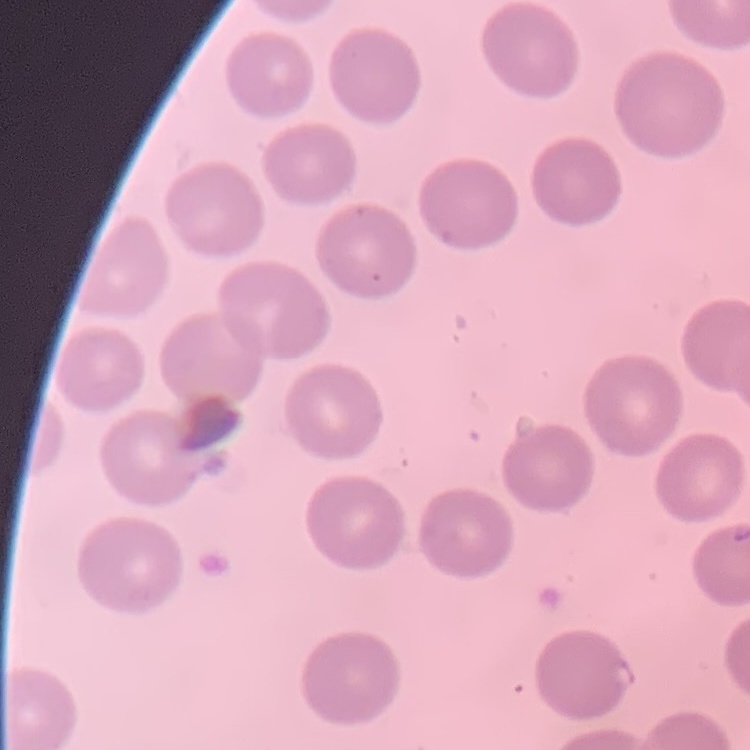

The red blood cells exhibit no rouleaux formation. Square crop of a larger photomicrograph. Field's or Giemsa stain. Thin blood smear.